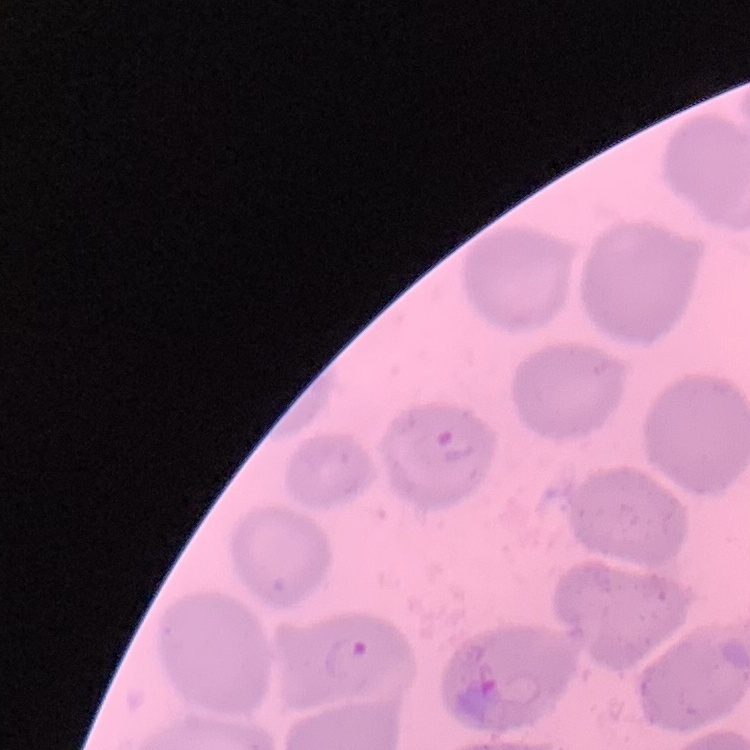

red blood cell morphology = no rouleaux formation
image type = square crop of a larger photomicrograph
preparation = thin blood smear
stain = Field's or Giemsa